Locate every blood parasite and identify its species.
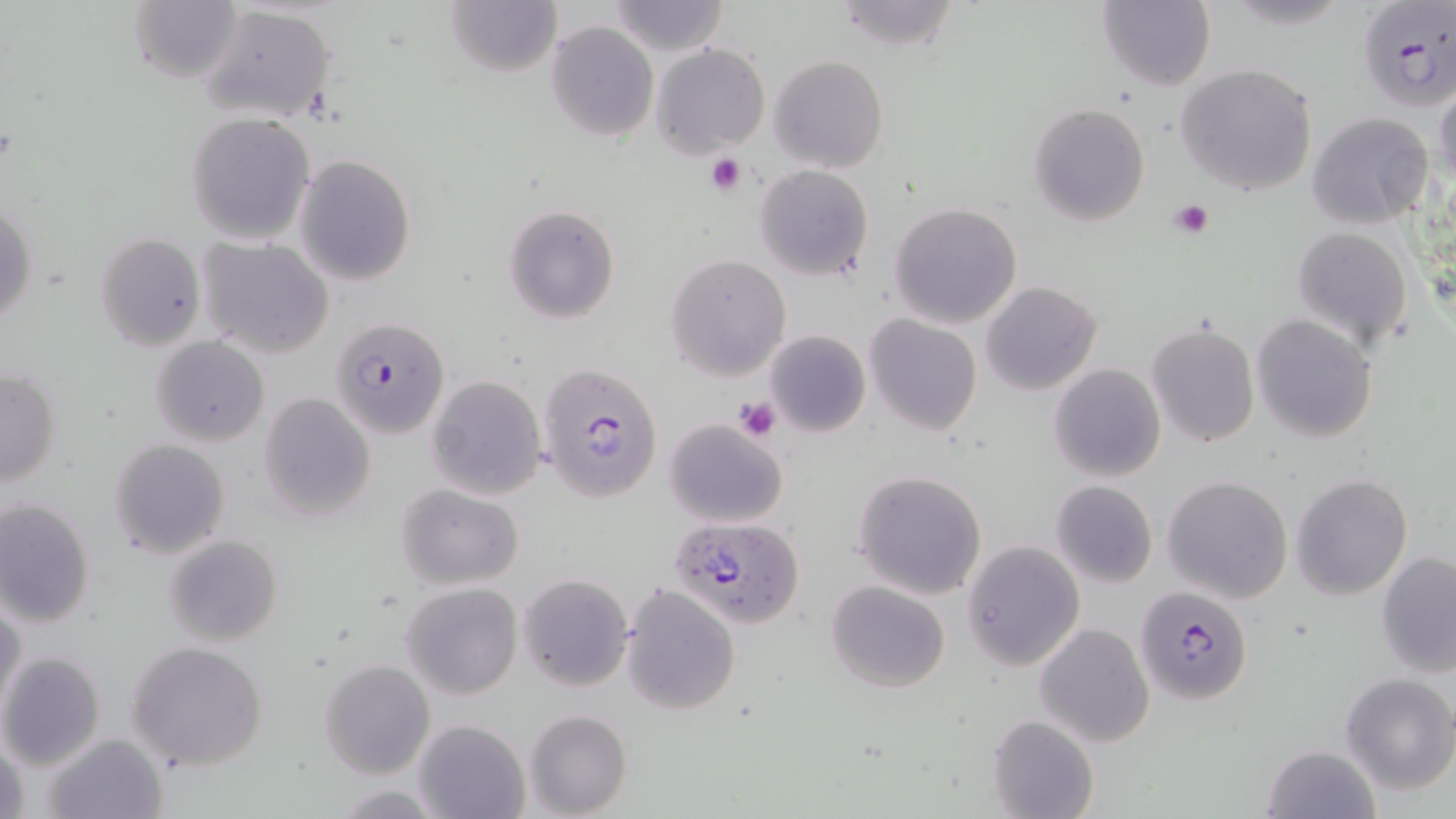
Approximate bounding boxes as [x1, y1, x2, y2] in pixels.
Plasmodium falciparum-infected red blood cells: [1358, 0, 1454, 110], [335, 320, 450, 441], [541, 361, 664, 502], [671, 513, 804, 626], [1140, 582, 1245, 705].
No Plasmodium ovale, Plasmodium malariae, Plasmodium vivax, Babesia divergens, or Trypanosoma brucei observed.

Summary:
  - Uninfected red blood cell locations: [129, 0, 243, 83], [605, 0, 731, 56], [1099, 0, 1216, 92], [443, 1, 562, 79], [833, 1, 962, 52], [200, 4, 336, 122], [545, 21, 659, 141], [651, 42, 770, 158], [770, 55, 888, 172], [1176, 63, 1317, 197], [1434, 85, 1456, 192], [1028, 102, 1149, 227], [184, 112, 316, 245], [1307, 112, 1434, 226], [295, 154, 416, 286], [755, 165, 873, 280], [1, 202, 36, 328], [889, 203, 1023, 328], [504, 205, 619, 323], [1293, 226, 1412, 349], [95, 233, 205, 351], [198, 235, 331, 356], [665, 254, 792, 380], [981, 281, 1102, 396], [1252, 313, 1377, 442], [864, 314, 982, 436], [1147, 322, 1260, 448], [764, 330, 871, 438], [151, 336, 270, 447], [1048, 363, 1165, 482], [1, 370, 61, 487], [426, 375, 547, 499], [257, 393, 376, 521], [665, 418, 787, 528], [108, 438, 232, 558], [853, 469, 987, 599], [1291, 473, 1412, 600], [1163, 476, 1293, 604], [1050, 480, 1158, 589], [396, 485, 524, 589], [0, 498, 96, 627], [164, 536, 283, 646], [962, 540, 1086, 670], [1377, 551, 1456, 677], [517, 574, 633, 691], [827, 580, 949, 693], [402, 583, 523, 698], [623, 583, 740, 716], [0, 597, 25, 717], [1036, 622, 1155, 747], [127, 640, 269, 772], [0, 652, 106, 770], [318, 659, 434, 780], [1339, 672, 1454, 793], [525, 710, 632, 818], [987, 714, 1097, 819], [413, 718, 531, 819], [42, 733, 168, 819], [1, 736, 31, 819], [1262, 744, 1380, 819], [331, 784, 447, 817]
  - Platelet locations: [704, 152, 748, 197], [1171, 198, 1215, 238], [732, 396, 782, 441]
  - Slide-level diagnosis: Plasmodium falciparum
  - Preparation: thin blood smear
  - Stain: May-Grünwald-Giemsa
  - Image size: 1456×819 pixels
  - Modality: light microscopy
  - Magnification: 1000x
  - Field of view: one of a larger specimen